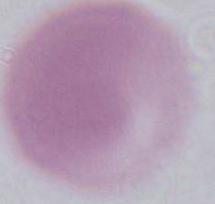
Summary:
  - Modality: photomicrograph
  - Magnification: 1000x
  - Identification: red blood cell